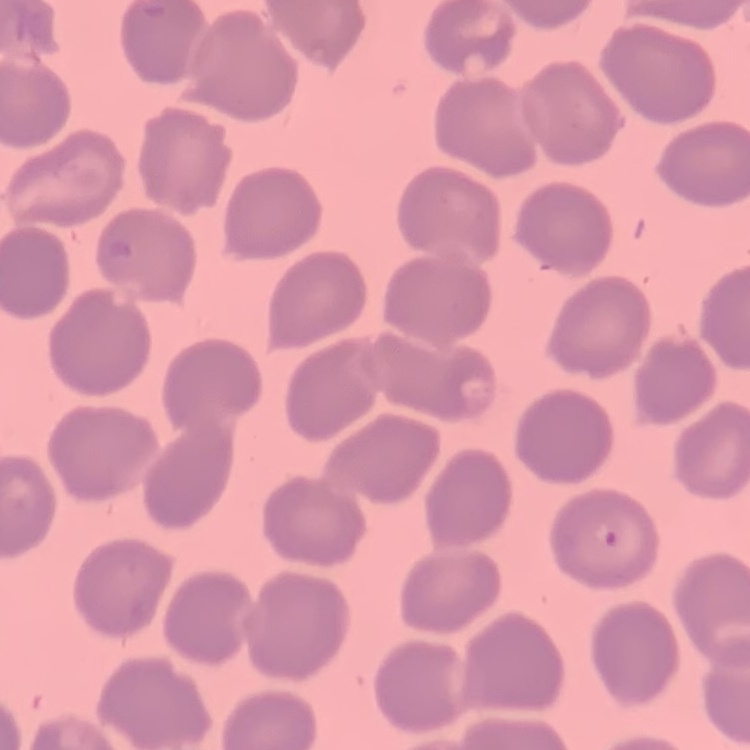
red blood cell morphology = no rouleaux formation
image type = square crop of a larger photomicrograph
preparation = thin peripheral smear
stain = Field's or Giemsa